Assess the morphology of the erythrocytes.
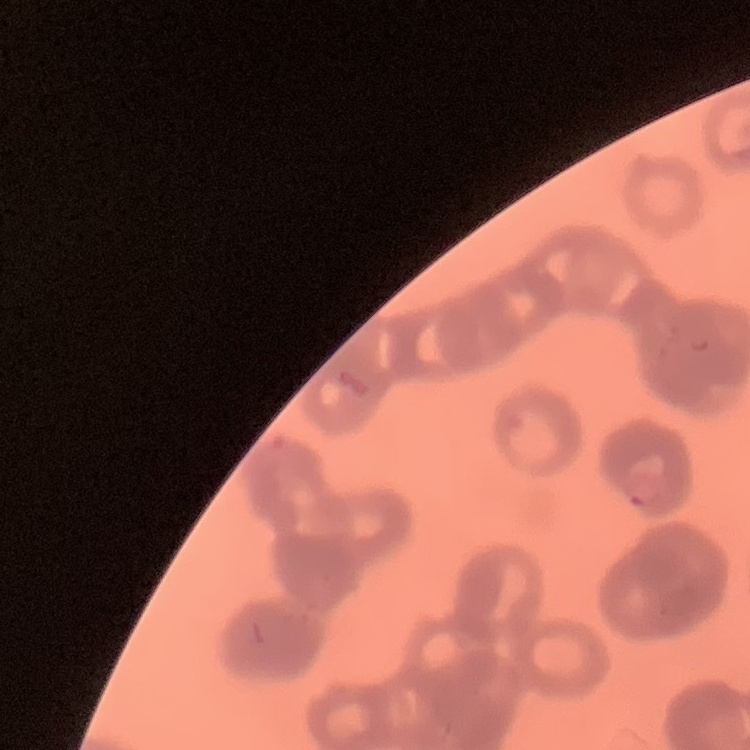
They show rouleaux formation.

Summary:
  - Stain: Field's or Giemsa
  - Preparation: thin blood film
  - Image type: square crop of a larger photomicrograph